Give the preparation type.
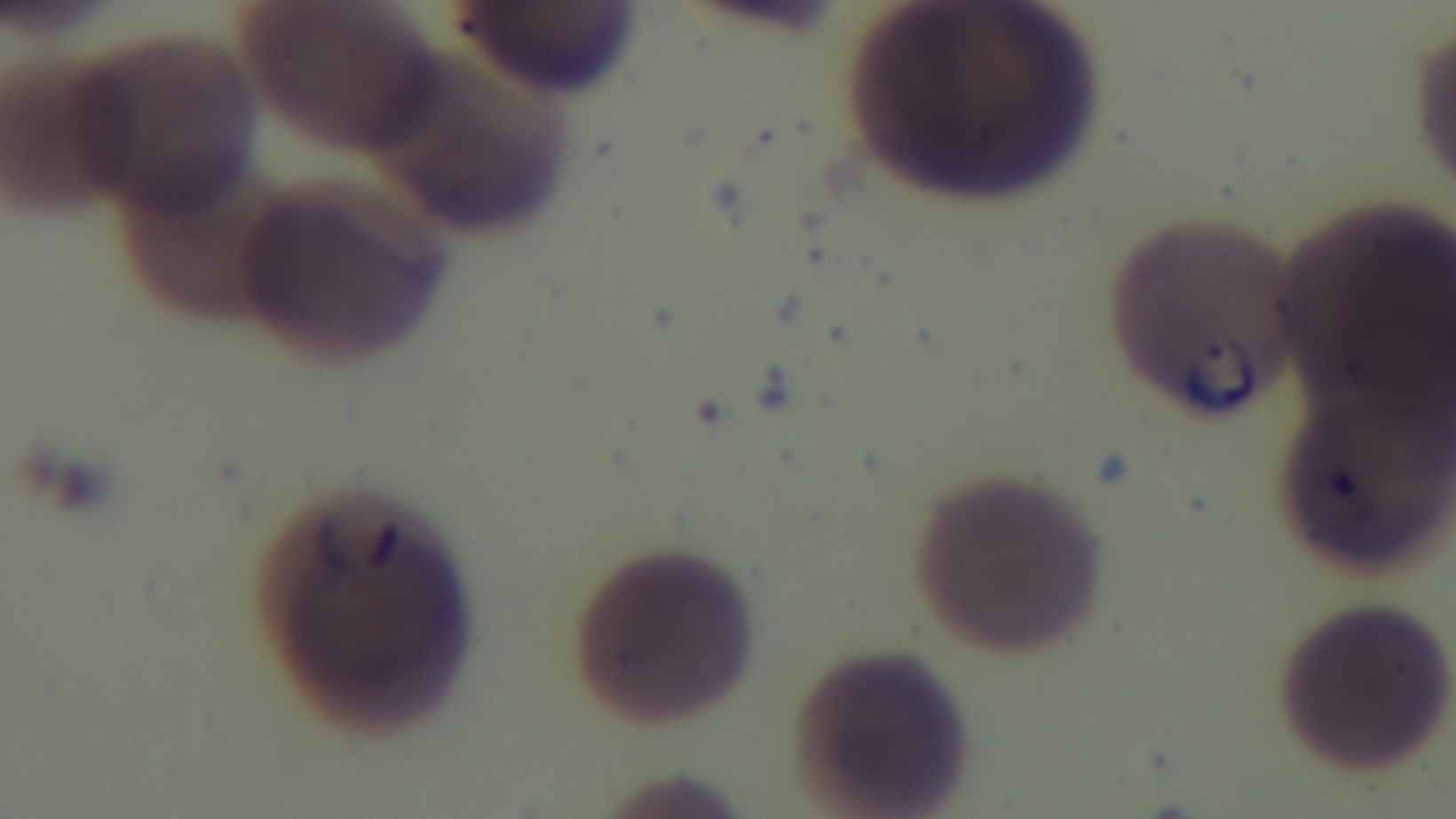

A thin smear.

stain = Giemsa
malaria status = infected
modality = light microscopy
field of view = one from the slide
objective = 100x oil immersion
capture = mounted 4K digital camera